Evaluate for Plasmodium parasites.
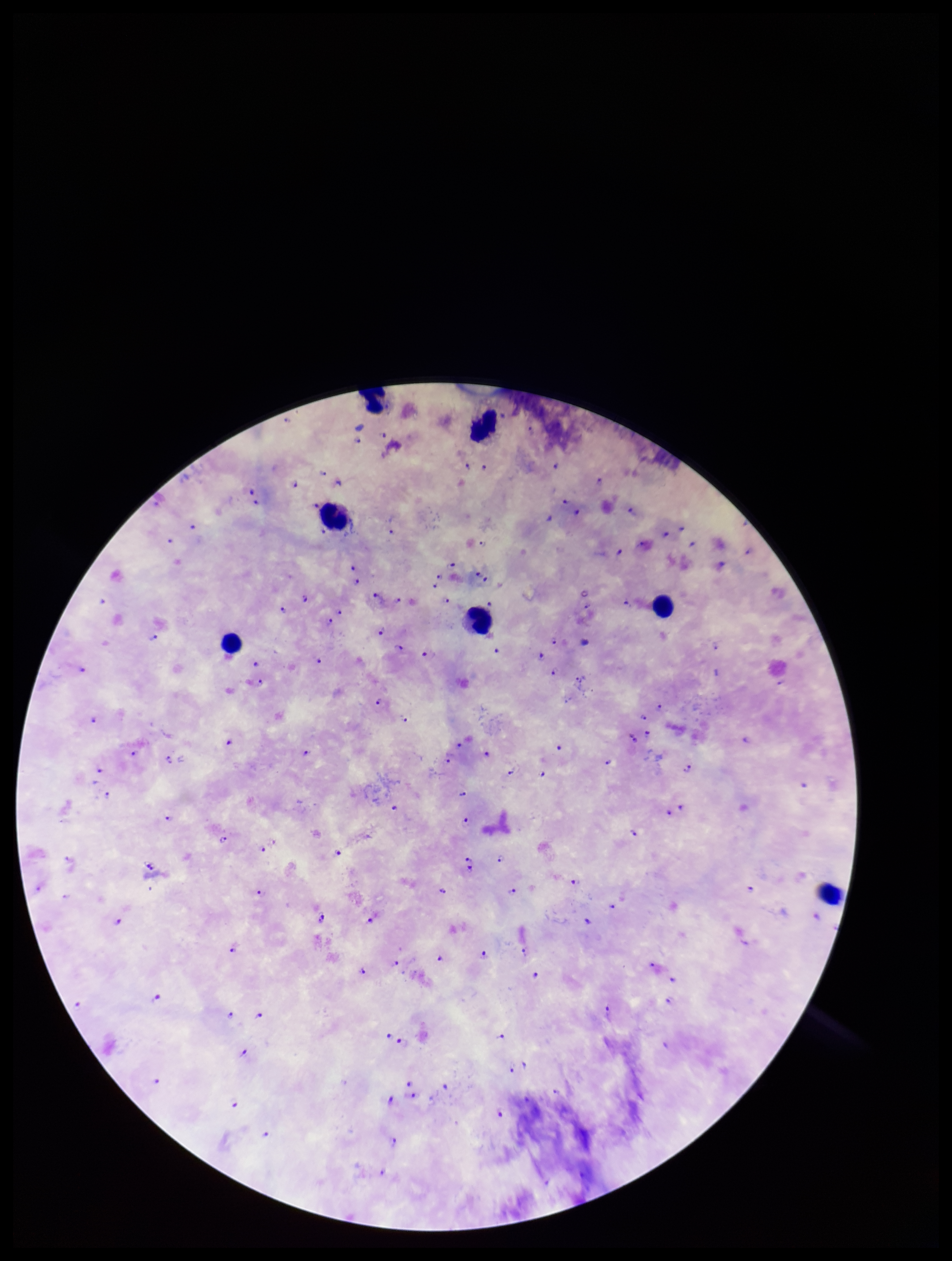
Identified.

Leukocyte count: 7. Photographed through the microscope eyepiece with a smartphone camera. Single field of view. Image is 952×1261 pixels. Stained with Giemsa. Parasite count: 97. Patient malaria status: positive. Preparation: thick blood smear. Species reported for this patient: Plasmodium falciparum.